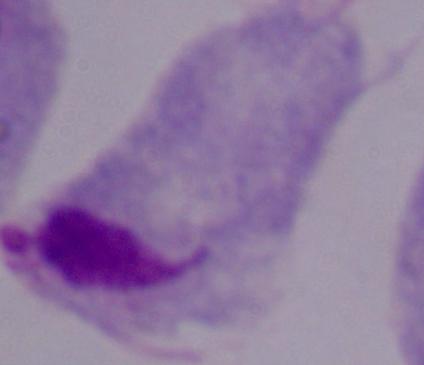

A trichomonad is seen. Micrograph. 1000x magnification.